Assess this cell for malaria.
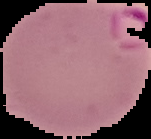

Parasitized.

Summary:
  - Image size: 151×139 pixels
  - Preparation: thin blood smear
  - Image type: segmented cell region on a black background